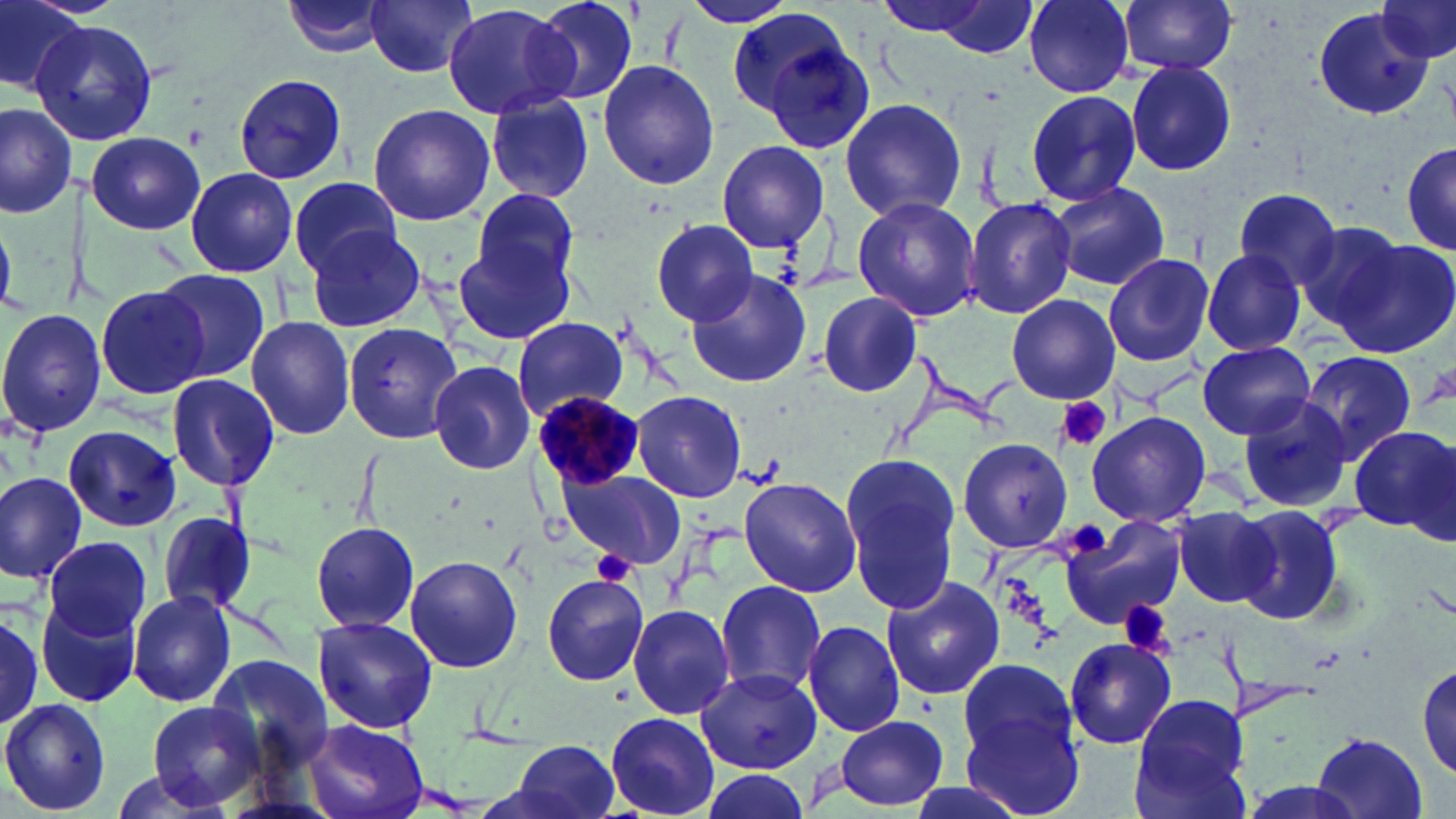
Approximate bounding boxes as [x1, y1, x2, y2] in pixels. Platelet locations: [1056, 396, 1113, 453], [1072, 521, 1106, 559], [593, 551, 636, 583], [1121, 600, 1170, 656]. Plasmodium malariae-infected red blood cell locations: [532, 390, 646, 491]. Uninfected red blood cell locations: [0, 0, 88, 97], [283, 0, 391, 58], [364, 0, 480, 79], [530, 0, 643, 108], [685, 0, 794, 28], [872, 0, 1020, 42], [923, 0, 1042, 58], [1025, 0, 1136, 95], [1114, 0, 1240, 76], [1375, 0, 1455, 65], [443, 2, 580, 121], [727, 7, 855, 118], [1313, 8, 1435, 121], [35, 19, 159, 147], [762, 36, 878, 154], [596, 59, 720, 190], [1125, 62, 1237, 176], [233, 72, 349, 186], [1025, 90, 1140, 205], [486, 96, 593, 201], [838, 96, 968, 222], [0, 102, 76, 221], [366, 104, 495, 226], [86, 130, 206, 236], [717, 141, 829, 250], [1398, 143, 1456, 257], [1400, 145, 1456, 255], [185, 167, 298, 276], [290, 176, 403, 276], [1049, 180, 1171, 289], [467, 186, 581, 302], [1230, 187, 1345, 291], [851, 197, 981, 322], [967, 197, 1076, 318], [1295, 218, 1410, 337], [649, 219, 760, 324], [304, 222, 429, 332], [1332, 236, 1456, 356], [450, 242, 572, 342], [1202, 250, 1308, 355], [1103, 252, 1215, 368], [687, 266, 813, 388], [153, 268, 269, 384], [94, 283, 209, 401], [817, 292, 923, 397], [1007, 294, 1120, 403], [0, 309, 107, 437], [245, 316, 357, 440], [514, 316, 628, 421], [342, 321, 464, 445], [1197, 343, 1315, 438], [1301, 351, 1417, 460], [428, 358, 534, 476], [167, 373, 280, 491], [630, 390, 748, 502], [1238, 397, 1356, 513], [1085, 410, 1210, 528], [64, 424, 182, 529], [1349, 427, 1454, 535], [957, 438, 1074, 553], [842, 456, 959, 612], [560, 468, 686, 568], [0, 471, 88, 586], [738, 476, 863, 597], [1233, 506, 1346, 628], [1171, 507, 1279, 608], [156, 512, 262, 615], [1061, 515, 1186, 630], [311, 520, 420, 635], [44, 535, 151, 642], [405, 554, 522, 674], [540, 572, 650, 685], [879, 576, 1006, 701], [714, 580, 829, 696], [128, 589, 238, 709], [536, 589, 733, 703], [36, 594, 143, 710], [626, 603, 735, 719], [0, 607, 45, 730], [0, 613, 45, 728], [312, 617, 440, 733], [803, 620, 906, 737], [1063, 636, 1174, 749], [207, 652, 333, 777], [953, 660, 1088, 812], [1416, 662, 1455, 781], [697, 668, 822, 774], [1126, 695, 1255, 819], [0, 700, 112, 816], [142, 701, 267, 812], [606, 712, 718, 817], [835, 714, 948, 810], [304, 720, 430, 819], [1314, 731, 1428, 818], [508, 738, 622, 819], [692, 768, 814, 819], [898, 778, 1029, 819]. Slide-level diagnosis: Plasmodium malariae. May-Grünwald-Giemsa stain. Captured at 1000x magnification. Light microscopy. Single field of view. Thin blood smear. Image is 1456×819 pixels.